Report the malaria status of this cell.
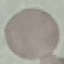
Uninfected.

Automatically extracted cell patch, resized to 64 × 64 pixels. Thin smear of blood. Giemsa-stained preparation. Acquired by smartphone through the microscope eyepiece.